Assess for Plasmodium parasites.
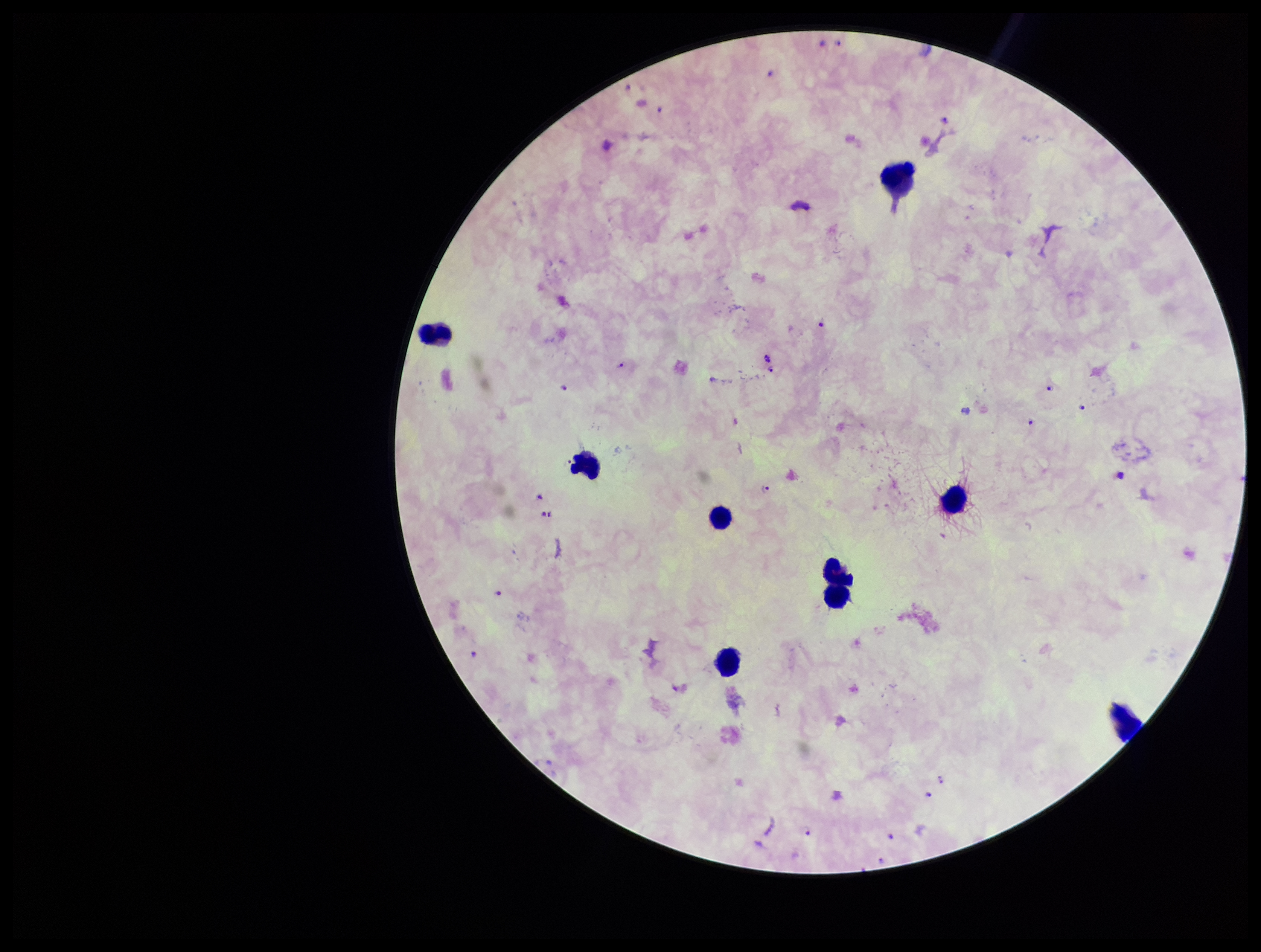

Seen.

parasite count = 16
image size = 1261×952 pixels
stain = Giemsa
preparation = thick
capture = smartphone photograph through the microscope eyepiece
field of view = one from this slide
patient malaria status = infected
leukocyte count = 8
species reported for this patient = Plasmodium falciparum